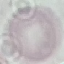

malaria_status: uninfected
stain: Giemsa
preparation: thin blood smear
capture: smartphone camera at the microscope eyepiece
image_type: cell patch, automatically extracted from a larger field of view and resized to 64 × 64 pixels